Look for parasitized red blood cells.
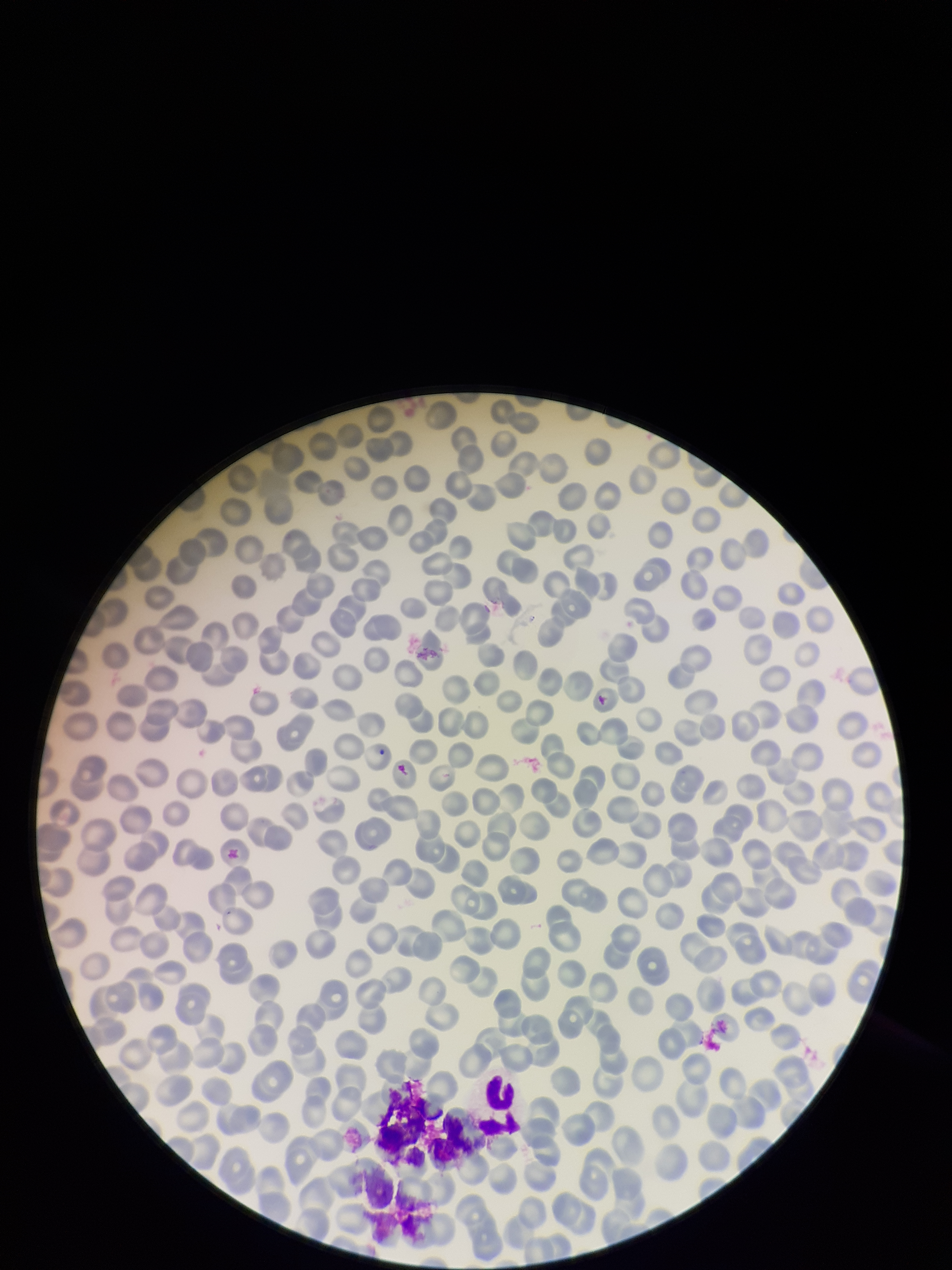
None seen.

Preparation: thin blood smear. Parasitized red blood cell count: 0. Red blood cell count: 229. Image is 952×1270 pixels. Patient malaria status: negative. Photographed through the microscope eyepiece with a smartphone camera. Stained with Giemsa. One field from this slide.